Report the malaria status of this cell.
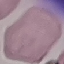
Uninfected.

image type = automatically extracted cell patch, resized to 64 × 64 pixels
capture = smartphone through the microscope eyepiece
preparation = thin blood film
stain = Giemsa